Name the cell type shown.
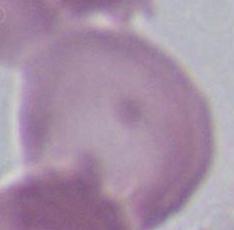

This is an erythrocyte.

1000x magnification. Photomicrograph.